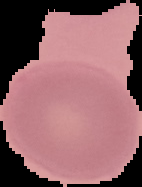
image size = 142×187 pixels
preparation = thin blood smear
malaria status = uninfected
image type = segmented cell region with the area outside set to black